Assess this cell for malaria.
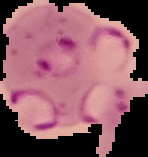
It is parasitized.

{
  "preparation": "thin blood smear",
  "image_type": "cell region segmented out of the field of view; surrounding area masked to black",
  "image_size": "148×157 pixels"
}